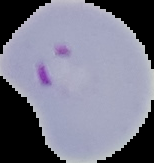
image size = 154×163 pixels
result = Plasmodium parasites detected
preparation = thin blood film
image type = cell region segmented out of the field of view; surrounding area masked to black